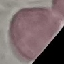
{
  "malaria_status": "uninfected",
  "stain": "Giemsa",
  "image_type": "cell patch, automatically extracted from a larger field of view and resized to 64 × 64 pixels",
  "preparation": "thin blood smear",
  "capture": "smartphone camera at the microscope eyepiece"
}